Name the blood parasite species.
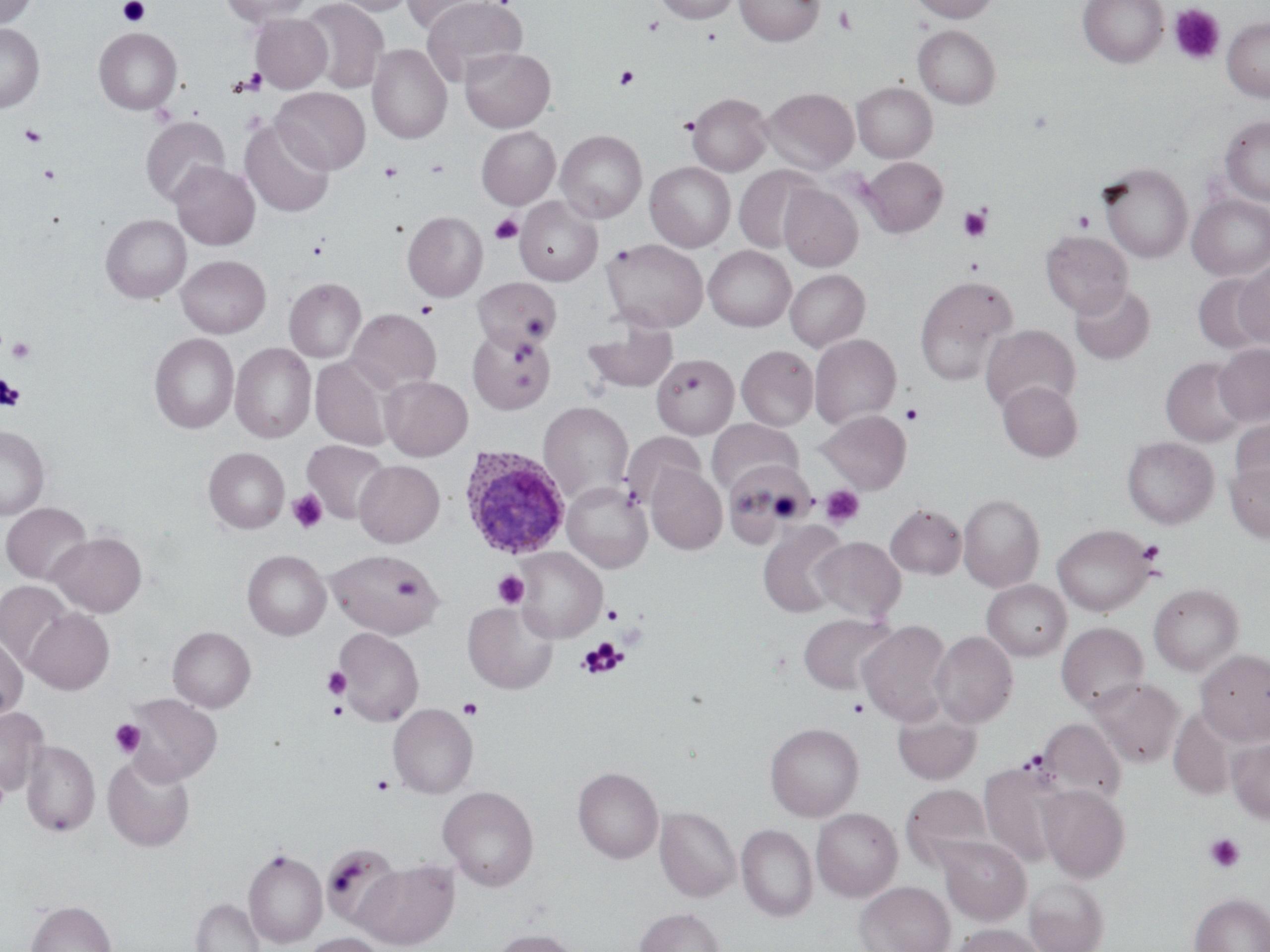
Plasmodium ovale.

Summary:
  - Coordinate format: approximate bounding boxes as named x1/y1/x2/y2 corners in pixels
  - Uninfected red blood cell locations: (x1=0, y1=0, x2=36, y2=28), (x1=220, y1=0, x2=311, y2=26), (x1=301, y1=0, x2=389, y2=93), (x1=331, y1=0, x2=413, y2=16), (x1=403, y1=0, x2=499, y2=35), (x1=421, y1=0, x2=527, y2=86), (x1=653, y1=0, x2=741, y2=23), (x1=735, y1=0, x2=825, y2=46), (x1=910, y1=0, x2=999, y2=23), (x1=1078, y1=0, x2=1169, y2=67), (x1=250, y1=13, x2=332, y2=93), (x1=1222, y1=16, x2=1270, y2=101), (x1=0, y1=23, x2=44, y2=113), (x1=913, y1=25, x2=1000, y2=109), (x1=93, y1=28, x2=182, y2=115), (x1=367, y1=44, x2=452, y2=144), (x1=459, y1=47, x2=555, y2=132), (x1=852, y1=81, x2=937, y2=162), (x1=761, y1=86, x2=859, y2=174), (x1=272, y1=87, x2=370, y2=174), (x1=687, y1=92, x2=773, y2=176), (x1=1220, y1=115, x2=1270, y2=206), (x1=141, y1=116, x2=229, y2=205), (x1=240, y1=119, x2=335, y2=218), (x1=476, y1=126, x2=560, y2=209), (x1=556, y1=130, x2=647, y2=223), (x1=860, y1=157, x2=947, y2=237), (x1=169, y1=161, x2=260, y2=250), (x1=645, y1=162, x2=735, y2=252), (x1=1098, y1=162, x2=1192, y2=263), (x1=734, y1=165, x2=822, y2=254), (x1=778, y1=184, x2=863, y2=271), (x1=1188, y1=194, x2=1270, y2=281), (x1=514, y1=197, x2=602, y2=285), (x1=403, y1=211, x2=488, y2=301), (x1=101, y1=214, x2=192, y2=303), (x1=1041, y1=230, x2=1133, y2=318), (x1=602, y1=238, x2=708, y2=333), (x1=703, y1=246, x2=796, y2=331), (x1=177, y1=255, x2=271, y2=338), (x1=1234, y1=261, x2=1270, y2=349), (x1=785, y1=269, x2=870, y2=352), (x1=1192, y1=274, x2=1269, y2=355), (x1=914, y1=275, x2=1018, y2=387), (x1=284, y1=277, x2=366, y2=362), (x1=473, y1=278, x2=560, y2=350), (x1=1070, y1=283, x2=1155, y2=365), (x1=347, y1=308, x2=441, y2=395), (x1=582, y1=319, x2=677, y2=393), (x1=980, y1=324, x2=1080, y2=414), (x1=467, y1=330, x2=556, y2=415), (x1=149, y1=333, x2=239, y2=433), (x1=809, y1=333, x2=901, y2=429), (x1=230, y1=342, x2=316, y2=443), (x1=1214, y1=343, x2=1270, y2=426), (x1=737, y1=345, x2=819, y2=430), (x1=652, y1=354, x2=739, y2=438), (x1=310, y1=356, x2=393, y2=451), (x1=1162, y1=357, x2=1249, y2=446), (x1=380, y1=375, x2=472, y2=460), (x1=997, y1=380, x2=1082, y2=461), (x1=538, y1=401, x2=633, y2=503), (x1=818, y1=410, x2=911, y2=493), (x1=1229, y1=418, x2=1270, y2=501), (x1=708, y1=419, x2=802, y2=493), (x1=0, y1=425, x2=50, y2=520), (x1=622, y1=431, x2=704, y2=507), (x1=1122, y1=436, x2=1219, y2=529), (x1=302, y1=440, x2=390, y2=524), (x1=203, y1=447, x2=289, y2=533), (x1=354, y1=460, x2=444, y2=547), (x1=1225, y1=461, x2=1270, y2=544), (x1=730, y1=462, x2=819, y2=554), (x1=646, y1=464, x2=727, y2=554), (x1=563, y1=482, x2=652, y2=572), (x1=958, y1=494, x2=1044, y2=591), (x1=1, y1=502, x2=92, y2=584), (x1=885, y1=504, x2=966, y2=578), (x1=758, y1=522, x2=848, y2=618), (x1=1054, y1=524, x2=1156, y2=616), (x1=48, y1=532, x2=147, y2=617), (x1=813, y1=537, x2=905, y2=621), (x1=514, y1=548, x2=606, y2=642), (x1=326, y1=549, x2=442, y2=638), (x1=243, y1=550, x2=331, y2=640), (x1=1, y1=580, x2=74, y2=668), (x1=982, y1=580, x2=1071, y2=661), (x1=1149, y1=583, x2=1243, y2=675), (x1=463, y1=601, x2=558, y2=694), (x1=24, y1=608, x2=114, y2=695), (x1=798, y1=613, x2=898, y2=696), (x1=857, y1=621, x2=952, y2=726), (x1=1056, y1=622, x2=1149, y2=713), (x1=168, y1=626, x2=255, y2=712), (x1=333, y1=627, x2=423, y2=726), (x1=930, y1=631, x2=1018, y2=727), (x1=0, y1=634, x2=28, y2=722), (x1=1196, y1=649, x2=1270, y2=746), (x1=1089, y1=678, x2=1185, y2=768), (x1=121, y1=692, x2=223, y2=786), (x1=388, y1=703, x2=478, y2=798), (x1=0, y1=707, x2=49, y2=796), (x1=892, y1=708, x2=982, y2=785), (x1=1169, y1=708, x2=1237, y2=800), (x1=1038, y1=718, x2=1126, y2=803), (x1=765, y1=722, x2=864, y2=821), (x1=1228, y1=736, x2=1270, y2=824), (x1=21, y1=739, x2=100, y2=837), (x1=22, y1=743, x2=190, y2=844), (x1=102, y1=753, x2=195, y2=852), (x1=0, y1=763, x2=9, y2=819), (x1=979, y1=763, x2=1064, y2=869), (x1=573, y1=766, x2=663, y2=863), (x1=902, y1=783, x2=993, y2=867), (x1=1038, y1=784, x2=1130, y2=882), (x1=438, y1=785, x2=539, y2=891), (x1=655, y1=806, x2=740, y2=902), (x1=811, y1=807, x2=902, y2=901), (x1=736, y1=824, x2=818, y2=921), (x1=939, y1=837, x2=1031, y2=924), (x1=243, y1=848, x2=327, y2=948), (x1=354, y1=858, x2=460, y2=950), (x1=1025, y1=878, x2=1109, y2=952), (x1=856, y1=881, x2=955, y2=952), (x1=1190, y1=892, x2=1270, y2=952), (x1=191, y1=899, x2=263, y2=952), (x1=26, y1=900, x2=116, y2=952), (x1=635, y1=908, x2=725, y2=952), (x1=951, y1=924, x2=1045, y2=952), (x1=491, y1=928, x2=581, y2=952), (x1=300, y1=933, x2=384, y2=952)
  - Plasmodium ovale-infected red blood cell locations: (x1=459, y1=445, x2=571, y2=559)
  - Platelet locations: (x1=118, y1=0, x2=150, y2=26), (x1=1169, y1=3, x2=1225, y2=66), (x1=834, y1=5, x2=857, y2=34), (x1=643, y1=16, x2=663, y2=36), (x1=615, y1=66, x2=639, y2=89), (x1=237, y1=68, x2=267, y2=95), (x1=19, y1=125, x2=47, y2=147), (x1=379, y1=161, x2=402, y2=183), (x1=40, y1=164, x2=62, y2=184), (x1=958, y1=205, x2=992, y2=243), (x1=1072, y1=211, x2=1095, y2=232), (x1=489, y1=213, x2=524, y2=245), (x1=964, y1=258, x2=984, y2=274), (x1=416, y1=302, x2=437, y2=318), (x1=6, y1=337, x2=36, y2=364), (x1=0, y1=375, x2=25, y2=410), (x1=901, y1=403, x2=923, y2=425), (x1=820, y1=486, x2=864, y2=528), (x1=287, y1=489, x2=327, y2=533), (x1=1137, y1=540, x2=1165, y2=565), (x1=493, y1=570, x2=529, y2=608), (x1=394, y1=575, x2=422, y2=599), (x1=603, y1=604, x2=622, y2=625), (x1=578, y1=638, x2=628, y2=678), (x1=322, y1=667, x2=350, y2=698), (x1=458, y1=698, x2=483, y2=720), (x1=847, y1=698, x2=870, y2=719), (x1=328, y1=701, x2=347, y2=719), (x1=110, y1=719, x2=146, y2=758), (x1=371, y1=774, x2=395, y2=795), (x1=1205, y1=834, x2=1245, y2=873)
  - Field of view: one of a larger specimen
  - Stain: May-Grünwald-Giemsa
  - Magnification: 1000x
  - Preparation: thin blood smear
  - Image size: 1270×952 pixels
  - Modality: optical microscopy